Classify the preparation.
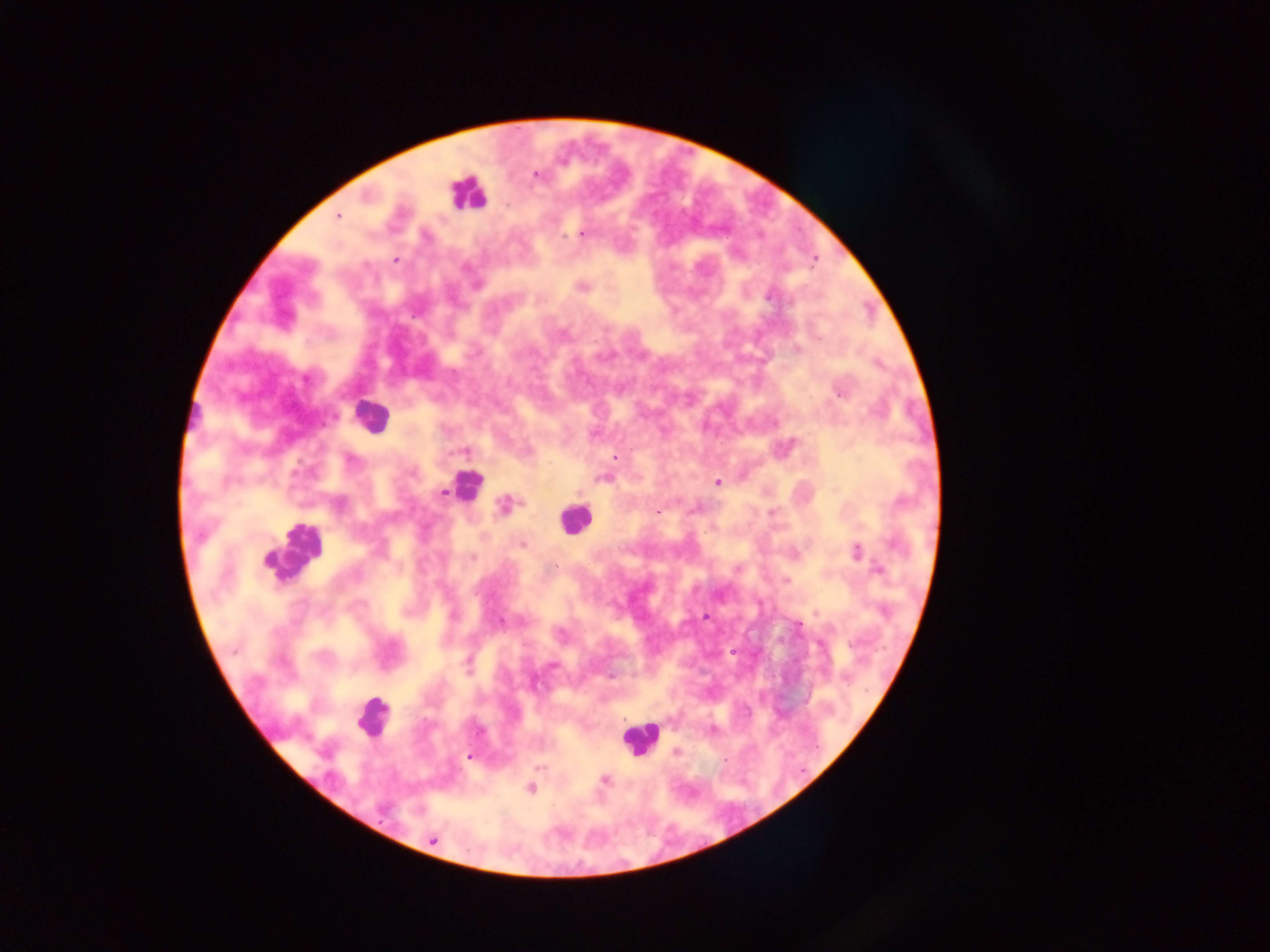

This is a thick smear.

Approximate centers as (x, y) in pixels.
Summary:
  - Leukocyte locations: (466, 193), (370, 414), (196, 418), (466, 486), (574, 520), (292, 550), (372, 717), (640, 738)
  - Plasmodium parasite locations: (536, 175), (338, 215), (583, 235), (426, 236), (395, 260), (583, 287), (768, 297), (563, 335), (797, 349), (306, 379), (839, 392), (464, 451), (614, 457), (351, 461), (413, 473), (603, 478), (717, 482), (444, 493), (503, 504), (340, 506), (658, 513), (521, 545), (856, 551), (472, 557), (878, 570), (786, 581), (453, 616), (705, 617), (500, 621), (799, 626), (468, 661), (552, 665), (846, 679), (479, 731), (676, 751), (470, 757), (725, 760), (540, 768), (604, 780), (531, 789), (433, 840)
  - Field of view: single
  - Country: Ghana
  - Image size: 1270×952 pixels
  - Capture: mobile-phone photograph through a microscope